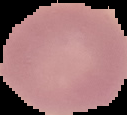
Cell region segmented out of the field of view; the surrounding area is masked to black. Image is 127×115 pixels. Result: no malaria parasites seen. From a thin blood smear.